Report the malaria status of this cell.
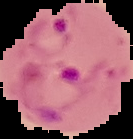
Parasitized.

Summary:
  - Image size: 133×139 pixels
  - Image type: segmented cell region with the area outside set to black
  - Preparation: thin blood film